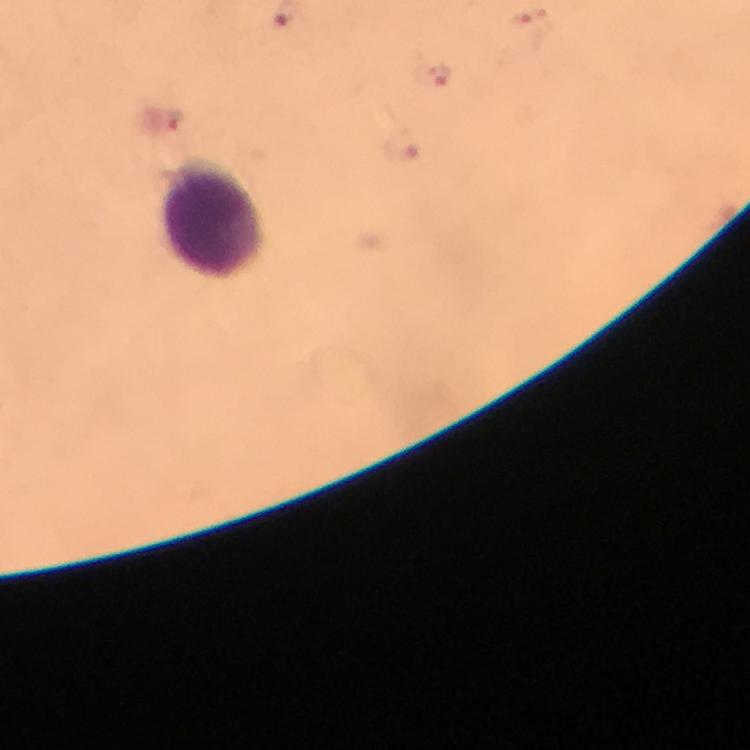

Approximate centers as {x, y} in pixels.
Summary:
  - Malaria parasite locations: {440, 73}, {174, 120}, {402, 146}
  - Leukocyte locations: {215, 219}
  - Magnification: 100x
  - Image size: 750×750 pixels
  - Cropped from: a single field of view
  - Preparation: thick blood smear
  - Context: from a malaria diagnostic workup
  - Immersion oil: applied
  - Capture: smartphone camera through the microscope
  - Stain: Giemsa